State which cell type is depicted.
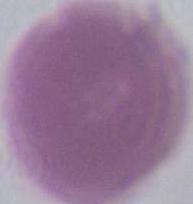

An erythrocyte.

{
  "modality": "photomicrograph",
  "magnification": "1000x"
}